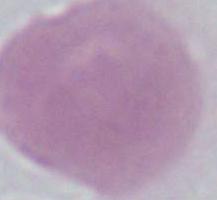

Micrograph. A red blood cell is shown. Captured at 1000x magnification.